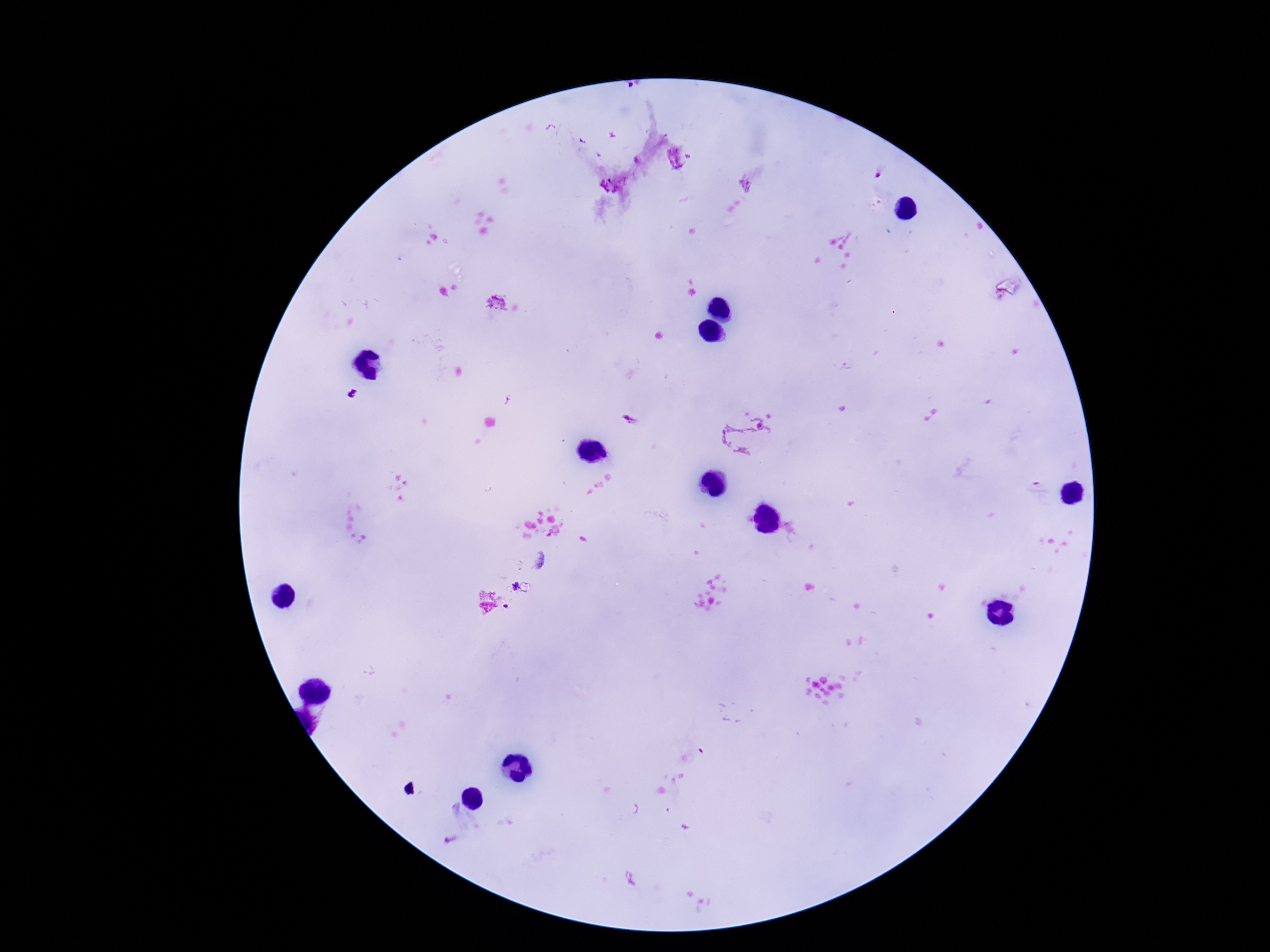

Approximate centers as (x, y) in pixels.
Summary:
  - Plasmodium parasite locations: (679, 158), (878, 175), (611, 185), (352, 394), (629, 419), (751, 436), (514, 585), (505, 607)
  - Patient malaria status: positive
  - Image size: 1270×952 pixels
  - Capture: smartphone camera through the microscope eyepiece
  - Preparation: thick blood film
  - Field of view: single
  - Stain: Giemsa
  - Magnification: 100x